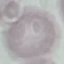 Result: no malaria parasites detected. Photographed with a smartphone camera at the microscope eyepiece. Automatically extracted cell patch, resized to 64 × 64 pixels. Giemsa stain. Thin blood film.